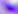

Micrograph. Toxoplasma gondii is seen. Captured at 400x magnification.